Identify the blood parasite species.
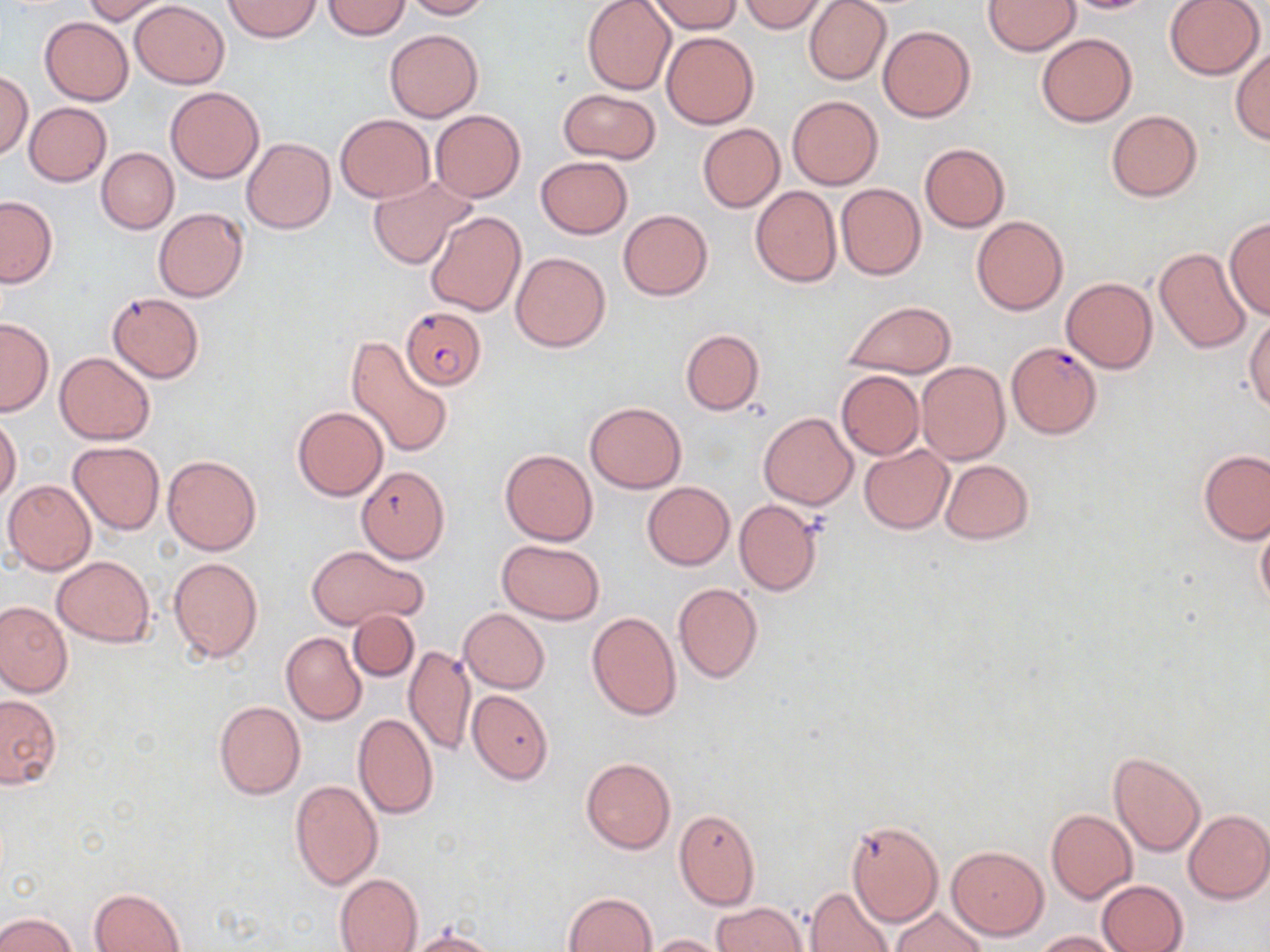
Plasmodium falciparum.

Approximate bounding boxes as named x1/y1/x2/y2 corners in pixels. Uninfected red blood cell locations: (x1=80, y1=0, x2=171, y2=23), (x1=224, y1=0, x2=322, y2=42), (x1=323, y1=0, x2=409, y2=39), (x1=402, y1=0, x2=492, y2=19), (x1=582, y1=0, x2=676, y2=95), (x1=648, y1=0, x2=742, y2=33), (x1=737, y1=0, x2=830, y2=32), (x1=984, y1=0, x2=1081, y2=55), (x1=1054, y1=0, x2=1162, y2=14), (x1=1163, y1=0, x2=1266, y2=79), (x1=131, y1=1, x2=229, y2=87), (x1=803, y1=1, x2=891, y2=86), (x1=40, y1=17, x2=132, y2=105), (x1=878, y1=25, x2=975, y2=122), (x1=385, y1=29, x2=483, y2=121), (x1=661, y1=31, x2=758, y2=129), (x1=1035, y1=34, x2=1137, y2=127), (x1=1229, y1=46, x2=1270, y2=145), (x1=0, y1=73, x2=32, y2=159), (x1=165, y1=86, x2=265, y2=182), (x1=558, y1=88, x2=661, y2=163), (x1=787, y1=95, x2=883, y2=189), (x1=24, y1=102, x2=111, y2=185), (x1=431, y1=110, x2=525, y2=202), (x1=1106, y1=111, x2=1203, y2=201), (x1=335, y1=115, x2=434, y2=202), (x1=697, y1=123, x2=785, y2=212), (x1=242, y1=138, x2=336, y2=234), (x1=920, y1=144, x2=1009, y2=232), (x1=97, y1=148, x2=179, y2=233), (x1=536, y1=156, x2=632, y2=239), (x1=367, y1=177, x2=473, y2=270), (x1=836, y1=183, x2=926, y2=280), (x1=750, y1=186, x2=841, y2=287), (x1=0, y1=196, x2=58, y2=287), (x1=152, y1=208, x2=248, y2=302), (x1=619, y1=209, x2=713, y2=299), (x1=425, y1=210, x2=525, y2=316), (x1=972, y1=215, x2=1068, y2=315), (x1=1224, y1=218, x2=1270, y2=320), (x1=1154, y1=246, x2=1251, y2=352), (x1=511, y1=252, x2=610, y2=352), (x1=1061, y1=277, x2=1157, y2=373), (x1=107, y1=292, x2=204, y2=382), (x1=842, y1=301, x2=956, y2=378), (x1=1245, y1=309, x2=1270, y2=412), (x1=0, y1=318, x2=53, y2=416), (x1=680, y1=329, x2=763, y2=414), (x1=346, y1=335, x2=455, y2=459), (x1=54, y1=352, x2=154, y2=444), (x1=915, y1=361, x2=1010, y2=466), (x1=836, y1=370, x2=924, y2=461), (x1=585, y1=401, x2=686, y2=493), (x1=292, y1=405, x2=388, y2=501), (x1=759, y1=412, x2=857, y2=509), (x1=0, y1=415, x2=21, y2=503), (x1=68, y1=441, x2=164, y2=534), (x1=860, y1=445, x2=953, y2=534), (x1=500, y1=449, x2=598, y2=545), (x1=1198, y1=449, x2=1270, y2=544), (x1=163, y1=454, x2=260, y2=555), (x1=939, y1=459, x2=1034, y2=545), (x1=356, y1=466, x2=450, y2=562), (x1=2, y1=479, x2=96, y2=574), (x1=642, y1=481, x2=734, y2=569), (x1=734, y1=500, x2=823, y2=597), (x1=1255, y1=514, x2=1270, y2=612), (x1=497, y1=539, x2=605, y2=624), (x1=308, y1=545, x2=427, y2=629), (x1=51, y1=556, x2=155, y2=645), (x1=168, y1=557, x2=264, y2=661), (x1=673, y1=583, x2=763, y2=682), (x1=0, y1=599, x2=73, y2=697), (x1=459, y1=608, x2=550, y2=693), (x1=347, y1=610, x2=419, y2=682), (x1=587, y1=611, x2=682, y2=720), (x1=281, y1=632, x2=366, y2=724), (x1=405, y1=646, x2=474, y2=756), (x1=468, y1=689, x2=554, y2=784), (x1=0, y1=694, x2=62, y2=789), (x1=214, y1=701, x2=305, y2=798), (x1=353, y1=712, x2=438, y2=820), (x1=1108, y1=750, x2=1206, y2=857), (x1=581, y1=757, x2=676, y2=854), (x1=290, y1=779, x2=384, y2=890), (x1=674, y1=809, x2=761, y2=909), (x1=1046, y1=810, x2=1137, y2=902), (x1=1183, y1=810, x2=1270, y2=903), (x1=845, y1=820, x2=944, y2=926), (x1=948, y1=846, x2=1047, y2=939), (x1=334, y1=873, x2=423, y2=952), (x1=1097, y1=879, x2=1190, y2=952), (x1=806, y1=887, x2=894, y2=952), (x1=91, y1=888, x2=185, y2=952), (x1=563, y1=892, x2=657, y2=952), (x1=710, y1=902, x2=808, y2=952), (x1=890, y1=906, x2=987, y2=952), (x1=0, y1=911, x2=79, y2=952), (x1=403, y1=929, x2=499, y2=952), (x1=1037, y1=930, x2=1125, y2=951), (x1=645, y1=933, x2=732, y2=952). Plasmodium falciparum-infected red blood cell locations: (x1=400, y1=306, x2=488, y2=391), (x1=1006, y1=342, x2=1101, y2=439). Single field of view. Thin blood smear. 1000x magnification. Light microscopy. May-Grünwald-Giemsa stain. Image is 1270×952 pixels.